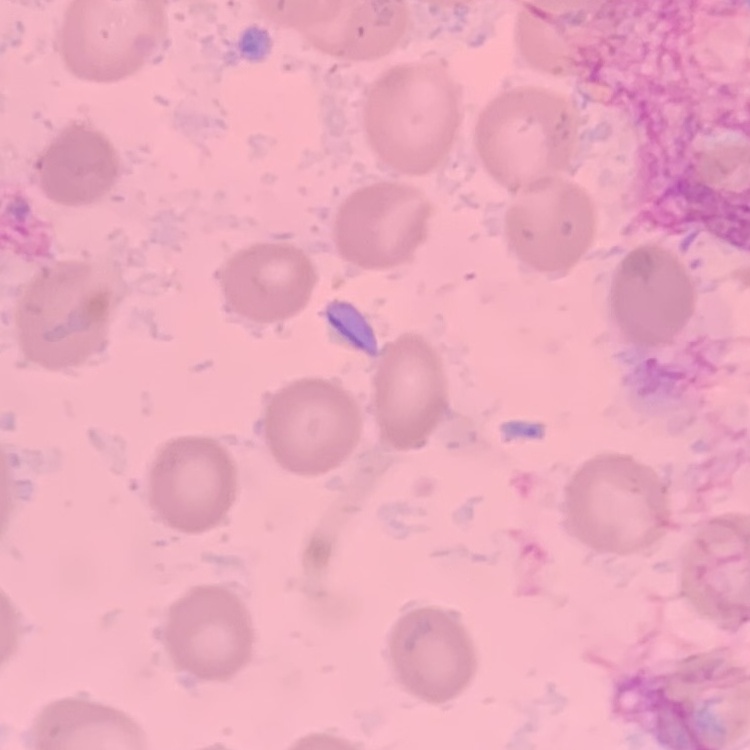
Summary:
  - Red blood cell morphology: no rouleaux formation
  - Preparation: thin blood film
  - Image type: square crop of a larger photomicrograph
  - Stain: Field's or Giemsa